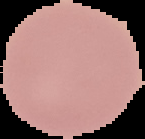
Summary:
  - Image type: cell region segmented out of the field of view; surrounding area masked to black
  - Image size: 145×139 pixels
  - Malaria status: uninfected
  - Preparation: thin blood smear